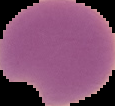

Cell region segmented out of the field of view; the surrounding area is masked to black. From a thin blood smear. Result: malaria parasites identified. Image is 115×106 pixels.